Point out every malaria parasite and every leukocyte.
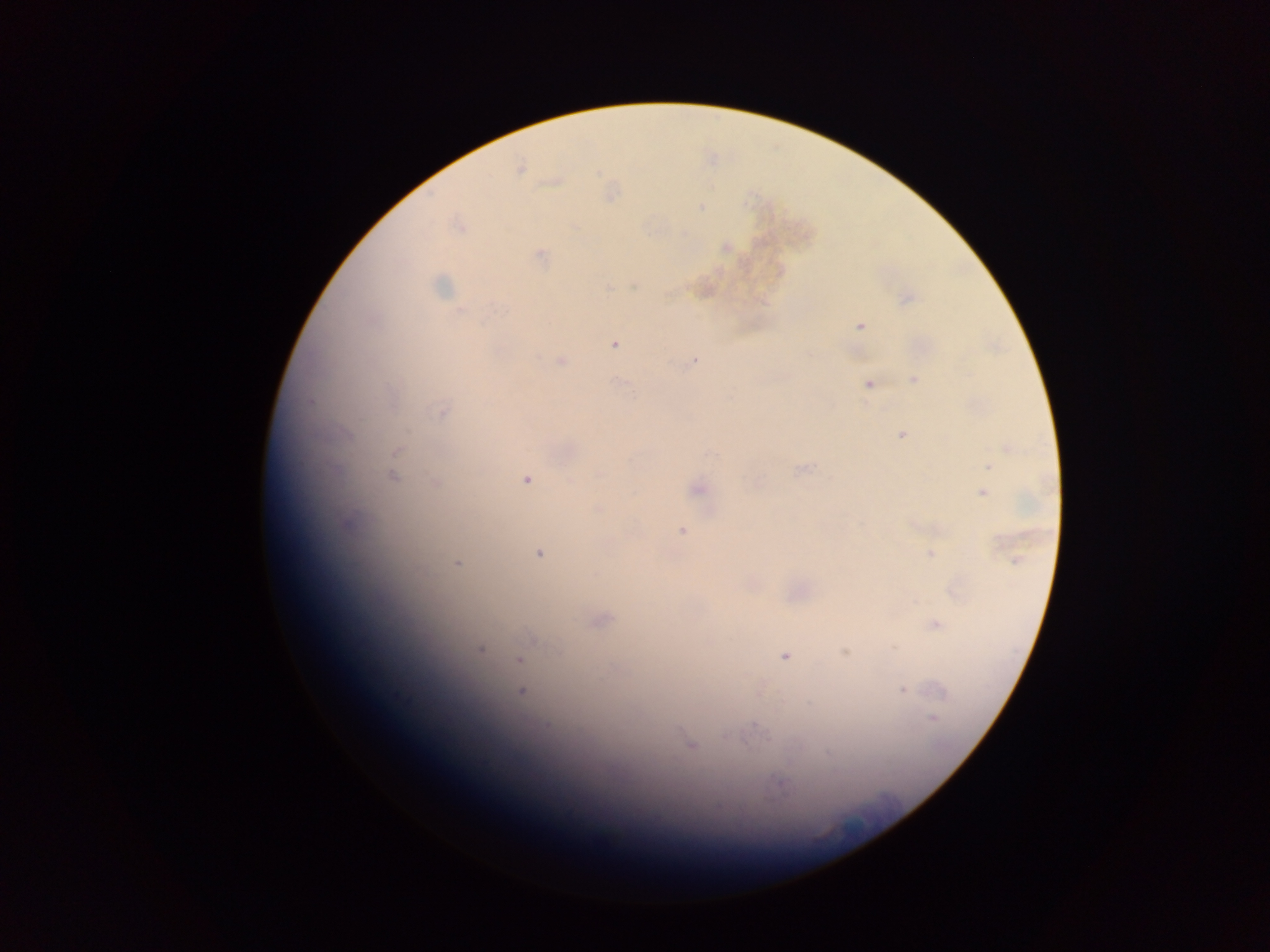
Approximate centers as (x, y) in pixels.
Malaria parasites: (520, 167), (701, 207), (459, 225), (725, 248), (540, 256), (441, 285), (635, 286), (607, 287), (460, 311), (860, 325), (614, 344), (560, 361), (693, 362), (914, 380), (867, 384), (442, 412), (901, 435), (1008, 449), (396, 452), (988, 467), (801, 469), (599, 475), (393, 477), (527, 480), (435, 482), (697, 489), (982, 493), (597, 509), (682, 531), (539, 554), (931, 555), (1016, 560), (457, 563), (602, 621), (935, 624), (480, 649), (895, 649), (558, 651), (845, 652), (784, 656), (518, 659), (902, 690), (521, 691), (933, 718), (547, 725), (756, 725), (691, 745).
No leukocytes observed.

Thick blood film. Image is 1270×952 pixels. Sample from Ghana. Mobile-phone photograph taken through the microscope. One field of view.